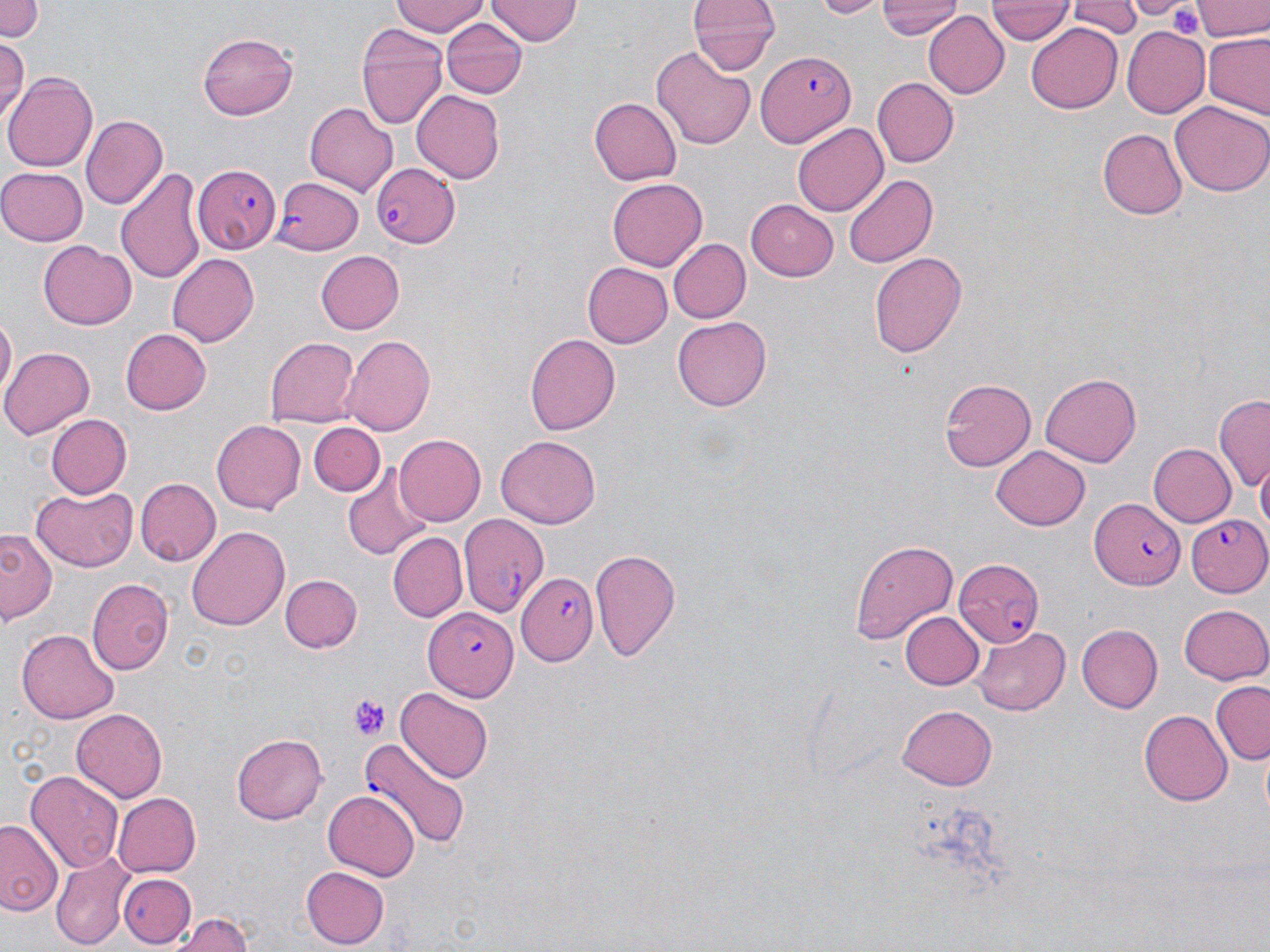 Approximate bounding boxes as named x1/y1/x2/y2 corners in pixels. Platelet locations: (x1=1171, y1=4, x2=1205, y2=38), (x1=349, y1=695, x2=391, y2=741). Uninfected red blood cell locations: (x1=0, y1=0, x2=46, y2=43), (x1=392, y1=0, x2=488, y2=37), (x1=486, y1=0, x2=580, y2=45), (x1=812, y1=0, x2=881, y2=17), (x1=876, y1=0, x2=960, y2=41), (x1=1067, y1=0, x2=1143, y2=42), (x1=1118, y1=0, x2=1192, y2=20), (x1=1192, y1=0, x2=1270, y2=42), (x1=987, y1=2, x2=1073, y2=46), (x1=690, y1=4, x2=779, y2=77), (x1=922, y1=9, x2=1008, y2=100), (x1=440, y1=17, x2=527, y2=100), (x1=355, y1=22, x2=451, y2=132), (x1=1027, y1=25, x2=1122, y2=113), (x1=1121, y1=25, x2=1211, y2=119), (x1=196, y1=31, x2=298, y2=120), (x1=1202, y1=34, x2=1270, y2=118), (x1=0, y1=39, x2=28, y2=122), (x1=651, y1=47, x2=758, y2=149), (x1=5, y1=70, x2=99, y2=173), (x1=871, y1=77, x2=957, y2=168), (x1=411, y1=90, x2=504, y2=183), (x1=589, y1=98, x2=682, y2=185), (x1=1171, y1=99, x2=1270, y2=196), (x1=306, y1=101, x2=400, y2=194), (x1=83, y1=114, x2=166, y2=208), (x1=793, y1=124, x2=887, y2=216), (x1=1098, y1=130, x2=1187, y2=218), (x1=0, y1=167, x2=89, y2=246), (x1=116, y1=167, x2=210, y2=282), (x1=841, y1=174, x2=939, y2=270), (x1=607, y1=178, x2=708, y2=270), (x1=745, y1=200, x2=839, y2=281), (x1=39, y1=238, x2=136, y2=327), (x1=666, y1=238, x2=749, y2=324), (x1=167, y1=251, x2=259, y2=343), (x1=315, y1=251, x2=405, y2=333), (x1=867, y1=252, x2=968, y2=358), (x1=582, y1=260, x2=673, y2=347), (x1=673, y1=313, x2=770, y2=408), (x1=0, y1=315, x2=16, y2=405), (x1=120, y1=328, x2=211, y2=415), (x1=343, y1=334, x2=436, y2=434), (x1=526, y1=334, x2=619, y2=435), (x1=265, y1=335, x2=359, y2=427), (x1=3, y1=345, x2=96, y2=439), (x1=1040, y1=372, x2=1142, y2=466), (x1=939, y1=377, x2=1037, y2=470), (x1=1214, y1=395, x2=1270, y2=492), (x1=44, y1=413, x2=132, y2=500), (x1=212, y1=420, x2=305, y2=514), (x1=308, y1=423, x2=384, y2=498), (x1=393, y1=433, x2=486, y2=526), (x1=495, y1=434, x2=602, y2=528), (x1=1150, y1=443, x2=1236, y2=527), (x1=991, y1=445, x2=1089, y2=530), (x1=1257, y1=460, x2=1269, y2=546), (x1=344, y1=467, x2=432, y2=558), (x1=136, y1=478, x2=221, y2=566), (x1=30, y1=486, x2=138, y2=572), (x1=186, y1=524, x2=290, y2=631), (x1=1, y1=526, x2=60, y2=627), (x1=389, y1=532, x2=467, y2=623), (x1=849, y1=539, x2=957, y2=645), (x1=588, y1=548, x2=683, y2=662), (x1=281, y1=574, x2=363, y2=653), (x1=87, y1=578, x2=172, y2=674), (x1=1179, y1=604, x2=1270, y2=686), (x1=901, y1=612, x2=983, y2=690), (x1=972, y1=624, x2=1072, y2=715), (x1=1074, y1=624, x2=1161, y2=712), (x1=18, y1=628, x2=119, y2=724), (x1=1212, y1=680, x2=1270, y2=766), (x1=396, y1=688, x2=493, y2=783), (x1=895, y1=705, x2=998, y2=789), (x1=72, y1=708, x2=168, y2=801), (x1=1138, y1=710, x2=1230, y2=806), (x1=230, y1=731, x2=328, y2=825), (x1=26, y1=771, x2=122, y2=875), (x1=324, y1=790, x2=419, y2=881), (x1=111, y1=792, x2=201, y2=878), (x1=0, y1=819, x2=64, y2=921), (x1=51, y1=854, x2=131, y2=951), (x1=301, y1=867, x2=390, y2=948), (x1=117, y1=873, x2=195, y2=946), (x1=171, y1=909, x2=258, y2=952). Plasmodium falciparum-infected red blood cell locations: (x1=758, y1=47, x2=857, y2=147), (x1=371, y1=161, x2=460, y2=247), (x1=193, y1=164, x2=280, y2=255), (x1=272, y1=176, x2=363, y2=254), (x1=1090, y1=499, x2=1183, y2=589), (x1=451, y1=512, x2=543, y2=625), (x1=1185, y1=516, x2=1269, y2=596), (x1=955, y1=558, x2=1046, y2=648), (x1=520, y1=572, x2=599, y2=663), (x1=424, y1=605, x2=515, y2=699), (x1=357, y1=736, x2=473, y2=849). Slide-level diagnosis: Plasmodium falciparum. One field of a larger specimen. Optical microscopy. May-Grünwald-Giemsa stain. Thin blood smear. Image is 1270×952 pixels. Captured at 1000x magnification.